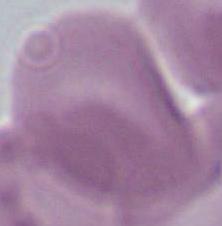 Micrograph. 1000x magnification. A red blood cell is shown.